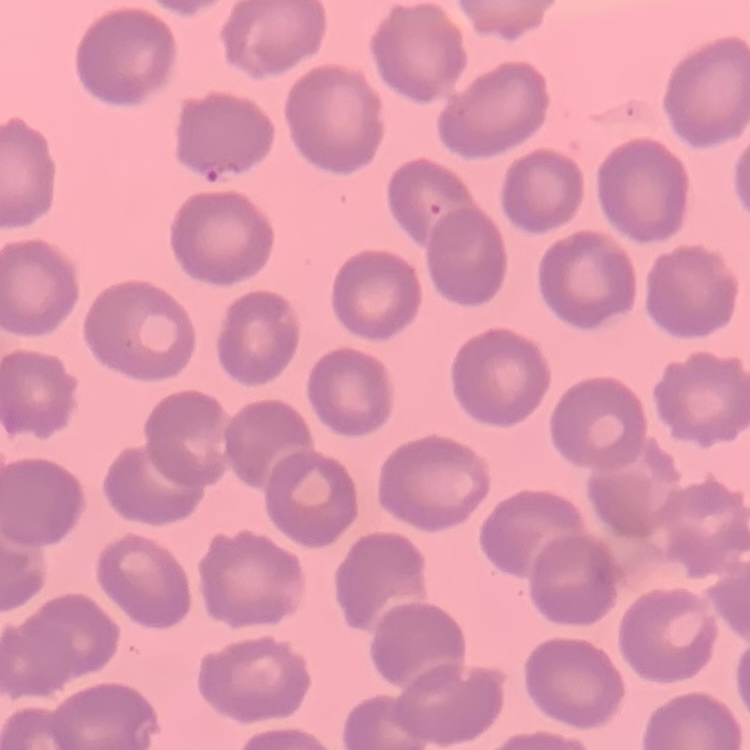
The erythrocytes show no rouleaux formation. Field's or Giemsa stain. Square crop of a larger photomicrograph. Thin blood film.